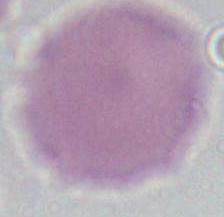
Summary:
  - Magnification: 1000x
  - Identification: red blood cell
  - Modality: photomicrograph